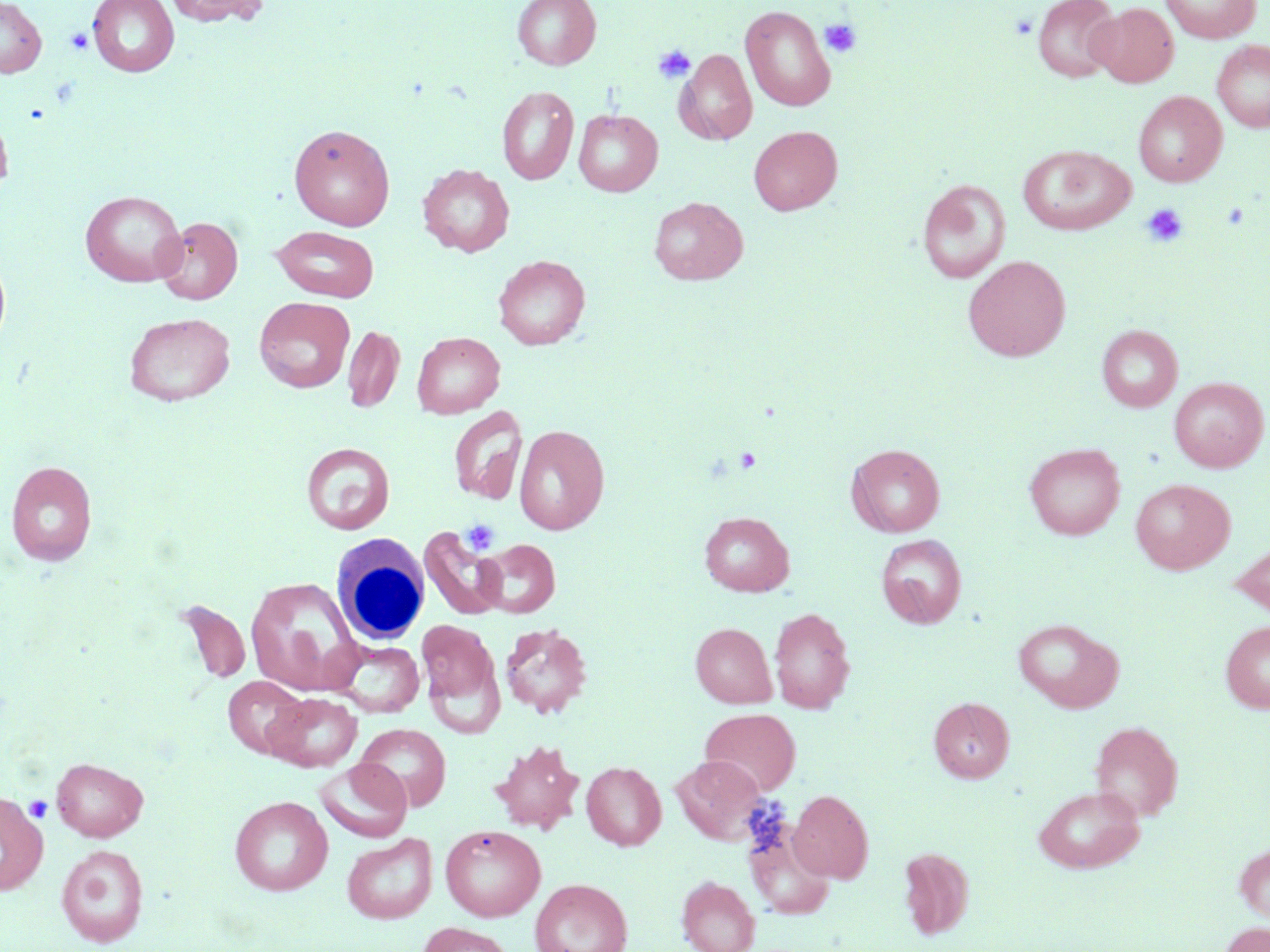

slide-level diagnosis = negative for blood parasites
platelet locations = approximate bounding boxes as (x1,y1)-(x2,y2) corner pairs in pixels: (1010,12)-(1038,40), (820,18)-(862,58), (65,28)-(93,55), (652,44)-(696,84), (1141,202)-(1188,248), (734,447)-(763,473), (461,519)-(500,555), (24,795)-(52,823)
image size = 1270×952 pixels
white blood cell locations = approximate bounding boxes as (x1,y1)-(x2,y2) corner pairs in pixels: (331,536)-(430,645)
uninfected red blood cell locations = approximate bounding boxes as (x1,y1)-(x2,y2) corner pairs in pixels: (0,0)-(47,77), (88,0)-(179,76), (166,0)-(267,28), (512,0)-(601,70), (1033,0)-(1121,82), (1160,0)-(1261,43), (1089,3)-(1178,87), (740,5)-(836,112), (1212,40)-(1270,132), (675,50)-(757,145), (496,86)-(579,185), (1133,91)-(1226,187), (0,108)-(14,201), (574,109)-(662,197), (289,124)-(395,231), (749,126)-(842,215), (1018,145)-(1135,235), (418,164)-(514,257), (917,179)-(1011,284), (80,189)-(187,286), (649,197)-(748,285), (155,216)-(243,304), (272,226)-(380,302), (0,249)-(12,357), (494,254)-(589,349), (963,255)-(1071,362), (254,296)-(355,393), (124,312)-(236,406), (1097,324)-(1183,412), (342,325)-(404,414), (412,332)-(505,418), (1169,377)-(1268,472), (448,405)-(527,506), (514,424)-(609,535), (301,442)-(395,534), (1024,442)-(1125,540), (847,443)-(945,537), (5,460)-(98,565), (1130,478)-(1235,574), (699,512)-(794,596), (418,525)-(508,621), (876,534)-(967,628), (478,539)-(560,618), (1230,540)-(1270,618), (246,576)-(363,697), (176,599)-(251,685), (769,607)-(855,714), (1014,617)-(1123,713), (417,620)-(498,709), (1220,620)-(1270,714), (500,621)-(593,718), (691,622)-(776,708), (333,640)-(424,717), (223,676)-(308,759), (265,693)-(362,772), (929,697)-(1014,782), (700,708)-(801,796), (1089,720)-(1183,821), (354,723)-(451,811), (490,740)-(585,833), (672,755)-(767,845), (51,757)-(148,841), (314,759)-(412,843), (582,761)-(666,850), (1032,785)-(1146,873), (789,789)-(873,883), (0,791)-(48,896), (229,795)-(333,895), (745,821)-(835,920), (440,825)-(546,921), (342,834)-(437,924), (1234,843)-(1270,923), (56,844)-(148,947), (898,847)-(975,940), (677,876)-(760,952), (531,878)-(633,952), (418,921)-(514,952), (1218,921)-(1270,952)
magnification = 1000x
modality = light microscopy
preparation = thin blood smear
stain = May-Grünwald-Giemsa
field of view = one of a larger specimen